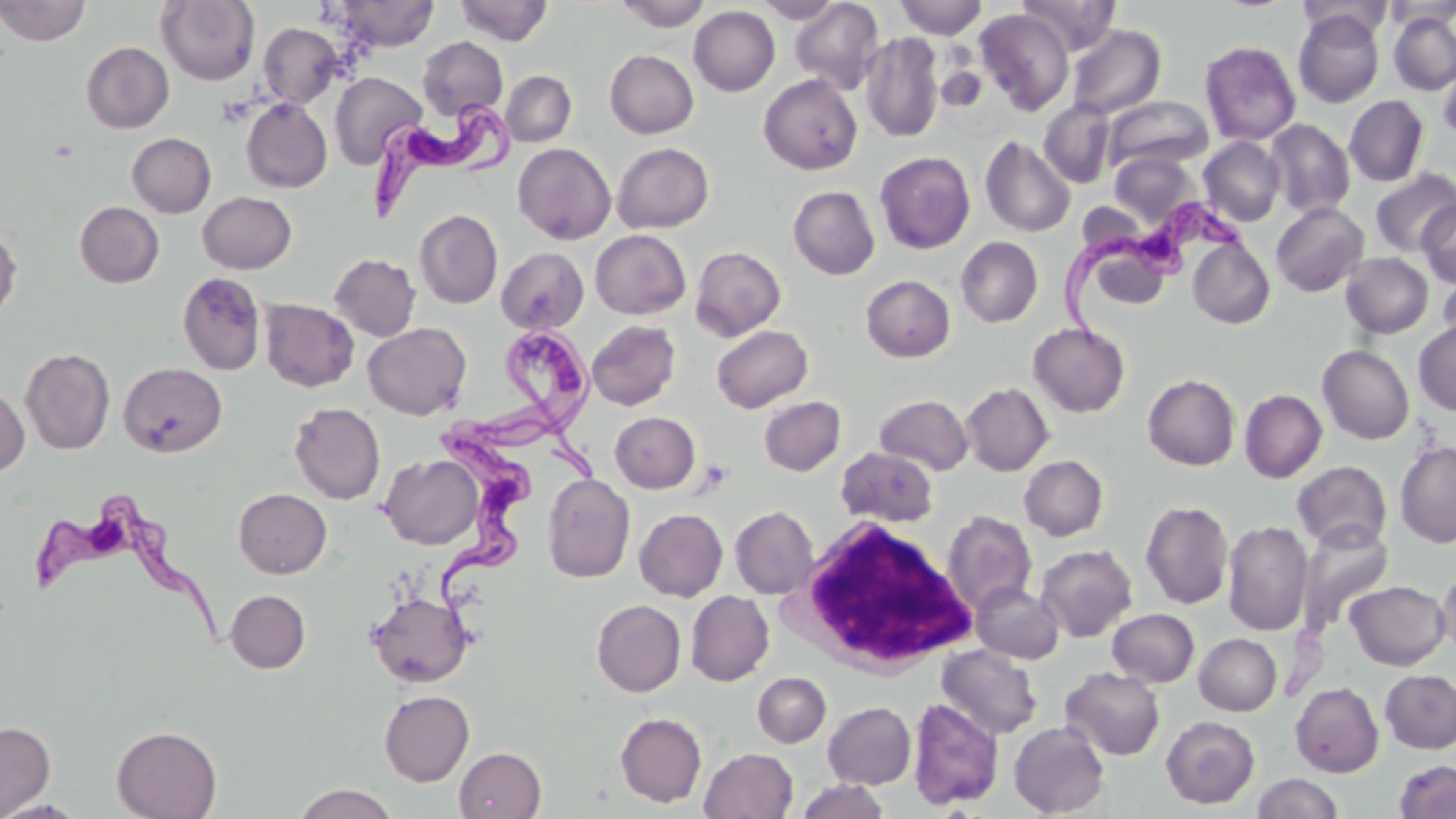

slide-level diagnosis = Trypanosoma brucei
white blood cell locations = approximate bounding boxes as [x1, y1, x2, y2] in pixels: [790, 515, 977, 673]
modality = optical microscopy
preparation = thin blood film
stain = May-Grünwald-Giemsa
magnification = 1000x
field of view = one of a larger specimen
Trypanosoma brucei locations = approximate bounding boxes as [x1, y1, x2, y2] in pixels: [369, 97, 520, 227], [1062, 196, 1248, 355], [445, 322, 607, 481], [420, 415, 532, 631], [31, 498, 228, 650]
image size = 1456×819 pixels
uninfected red blood cell locations = approximate bounding boxes as [x1, y1, x2, y2] in pixels: [0, 0, 90, 46], [156, 0, 259, 85], [333, 0, 439, 51], [618, 0, 710, 31], [752, 0, 845, 23], [894, 0, 986, 39], [1017, 0, 1121, 56], [1296, 0, 1393, 42], [1383, 0, 1456, 28], [455, 1, 553, 45], [790, 1, 885, 94], [689, 6, 780, 96], [975, 9, 1075, 115], [1294, 9, 1384, 108], [1388, 12, 1456, 95], [258, 22, 343, 108], [1066, 24, 1166, 119], [861, 32, 943, 142], [417, 36, 508, 121], [1200, 40, 1301, 145], [81, 42, 174, 133], [605, 49, 698, 138], [937, 62, 987, 111], [1437, 66, 1456, 144], [501, 71, 576, 147], [329, 72, 427, 170], [758, 74, 862, 175], [1345, 95, 1428, 187], [1104, 96, 1213, 173], [241, 98, 332, 193], [1038, 100, 1116, 188], [1265, 119, 1355, 218], [127, 132, 216, 217], [981, 135, 1076, 237], [1199, 137, 1286, 226], [612, 142, 714, 233], [513, 143, 615, 244], [875, 151, 975, 254], [1110, 153, 1198, 227], [1370, 169, 1456, 257], [788, 186, 880, 279], [197, 191, 296, 273], [1417, 200, 1455, 287], [75, 201, 164, 287], [1271, 202, 1369, 296], [414, 209, 503, 309], [0, 225, 21, 324], [590, 229, 690, 319], [956, 237, 1043, 327], [1188, 238, 1275, 329], [690, 245, 786, 341], [496, 247, 588, 333], [329, 253, 421, 341], [1340, 253, 1433, 339], [1438, 270, 1456, 356], [177, 272, 267, 375], [861, 275, 955, 362], [260, 299, 359, 391], [1413, 319, 1456, 416], [587, 320, 681, 410], [363, 322, 472, 420], [1028, 323, 1130, 417], [712, 324, 812, 413], [1317, 345, 1415, 444], [20, 348, 115, 454], [119, 362, 227, 457], [1143, 374, 1240, 470], [961, 382, 1053, 476], [0, 383, 30, 478], [1239, 389, 1327, 483], [874, 394, 973, 475], [759, 396, 846, 476], [289, 402, 385, 504], [610, 412, 700, 492], [1395, 441, 1456, 547], [836, 447, 938, 527], [380, 454, 483, 549], [1019, 455, 1108, 541], [1292, 461, 1391, 551], [542, 472, 635, 583], [233, 488, 332, 578], [1141, 500, 1233, 609], [730, 506, 818, 598], [634, 508, 728, 601], [942, 510, 1037, 613], [1223, 521, 1313, 635], [1296, 523, 1393, 634], [1036, 544, 1137, 642], [1434, 568, 1456, 659], [1344, 580, 1451, 670], [971, 582, 1063, 664], [225, 589, 310, 673], [686, 590, 774, 686], [367, 591, 473, 687], [591, 600, 686, 697], [1107, 608, 1199, 687], [1194, 633, 1281, 715], [937, 645, 1043, 739], [1061, 667, 1165, 760], [1380, 669, 1456, 753], [752, 672, 831, 748], [1290, 682, 1384, 777], [379, 690, 474, 786], [908, 697, 1004, 810], [823, 702, 916, 788], [615, 712, 706, 807], [1161, 715, 1259, 808], [0, 720, 56, 819], [1009, 721, 1110, 817], [111, 725, 222, 818], [454, 746, 546, 819], [700, 748, 798, 819], [1394, 759, 1456, 818], [1252, 773, 1343, 819], [797, 779, 889, 819], [292, 783, 399, 819]